Name the blood parasite species.
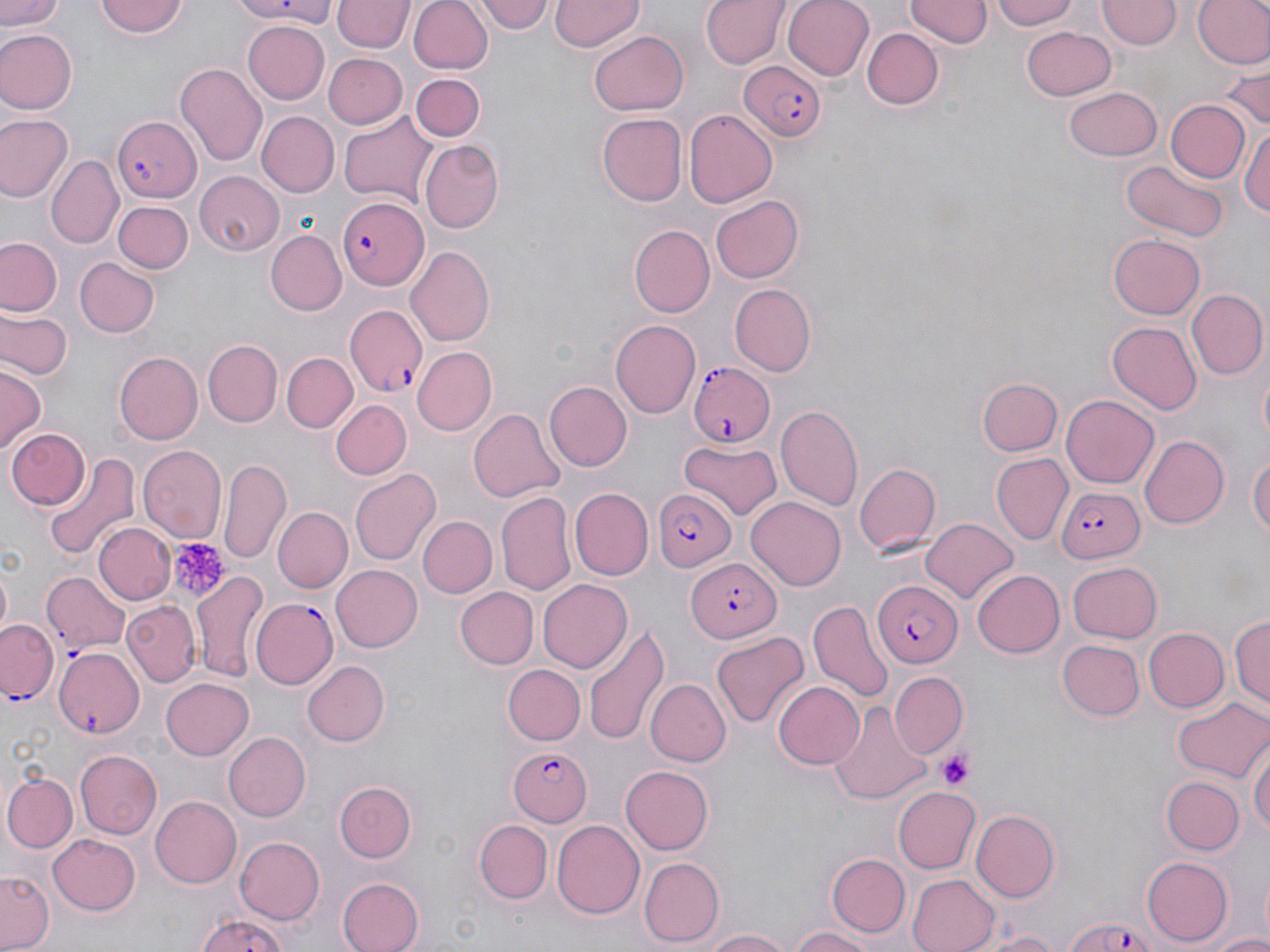
Plasmodium falciparum.

Approximate bounding boxes as (x1,y1)-(x2,y2) corner pairs in pixels. Uninfected red blood cell locations: (1,0)-(63,34), (96,0)-(191,40), (218,0)-(335,24), (408,0)-(494,75), (480,0)-(553,35), (551,0)-(643,50), (701,0)-(789,70), (782,0)-(877,82), (905,0)-(989,49), (989,0)-(1085,29), (1098,0)-(1180,51), (1192,0)-(1270,70), (333,1)-(412,53), (240,20)-(330,105), (1021,25)-(1117,101), (861,28)-(943,111), (0,29)-(76,112), (588,30)-(689,117), (321,52)-(407,129), (1219,62)-(1269,135), (175,63)-(266,168), (411,72)-(486,141), (1196,77)-(1266,173), (1063,86)-(1163,163), (1167,100)-(1249,182), (682,107)-(777,210), (257,111)-(338,197), (0,112)-(75,204), (339,112)-(440,204), (596,113)-(686,205), (1241,122)-(1270,223), (422,141)-(505,232), (49,155)-(123,250), (1121,159)-(1231,243), (193,170)-(284,255), (708,194)-(803,284), (112,200)-(192,273), (630,225)-(714,316), (266,231)-(345,316), (1109,232)-(1205,319), (1,236)-(62,317), (405,245)-(496,348), (74,257)-(160,338), (727,283)-(815,376), (1186,288)-(1269,382), (1,309)-(71,379), (610,318)-(701,419), (1105,320)-(1202,413), (203,340)-(283,426), (410,346)-(496,437), (114,351)-(203,444), (282,352)-(356,433), (1257,362)-(1270,454), (0,367)-(43,454), (978,378)-(1062,456), (545,382)-(632,470), (1059,394)-(1159,491), (330,400)-(412,481), (776,404)-(864,512), (469,407)-(565,504), (4,428)-(87,511), (1140,435)-(1228,528), (678,440)-(783,518), (137,445)-(227,541), (1248,449)-(1269,545), (43,452)-(140,563), (993,454)-(1074,545), (218,458)-(290,566), (852,461)-(940,556), (349,468)-(439,565), (569,488)-(652,581), (495,491)-(578,597), (746,496)-(848,590), (272,506)-(352,594), (417,516)-(497,599), (922,516)-(1018,604), (93,522)-(176,606), (1067,561)-(1163,644), (0,563)-(12,639), (330,564)-(423,652), (191,567)-(272,686), (971,569)-(1065,658), (538,578)-(633,673), (455,587)-(538,670), (808,596)-(893,701), (123,600)-(198,687), (1231,614)-(1270,712), (584,621)-(669,749), (1144,629)-(1228,712), (711,630)-(809,730), (1057,639)-(1145,722), (303,661)-(391,746), (504,666)-(584,745), (890,671)-(967,756), (161,675)-(255,760), (645,679)-(731,768), (771,681)-(864,769), (1171,698)-(1269,783), (828,699)-(932,808), (222,732)-(308,821), (1250,738)-(1268,844), (75,750)-(161,838), (621,765)-(714,855), (2,773)-(77,852), (1161,774)-(1244,853), (335,779)-(418,863), (893,788)-(980,873), (150,795)-(241,888), (967,806)-(1061,899), (474,820)-(552,903), (550,820)-(644,920), (49,834)-(140,916), (233,835)-(326,925), (825,852)-(910,938), (1141,856)-(1233,947), (640,857)-(723,946), (817,863)-(985,942), (1,869)-(55,951), (904,872)-(999,952), (336,874)-(424,952), (193,914)-(295,952), (786,925)-(883,952), (699,928)-(791,952), (977,930)-(1069,952), (1206,930)-(1270,951). Platelet locations: (167,536)-(230,603), (939,751)-(975,790). Plasmodium falciparum-infected red blood cell locations: (738,61)-(827,141), (110,115)-(199,202), (339,195)-(430,293), (344,303)-(428,396), (688,361)-(776,449), (1056,485)-(1146,563), (656,489)-(736,574), (686,558)-(781,642), (45,571)-(130,660), (875,579)-(963,669), (249,597)-(338,690), (0,620)-(58,704), (54,644)-(146,738), (505,748)-(592,825), (1063,918)-(1154,951). Single field of view. 1000x magnification. Optical microscopy. Image is 1270×952 pixels. Thin blood smear. May-Grünwald-Giemsa-stained preparation.